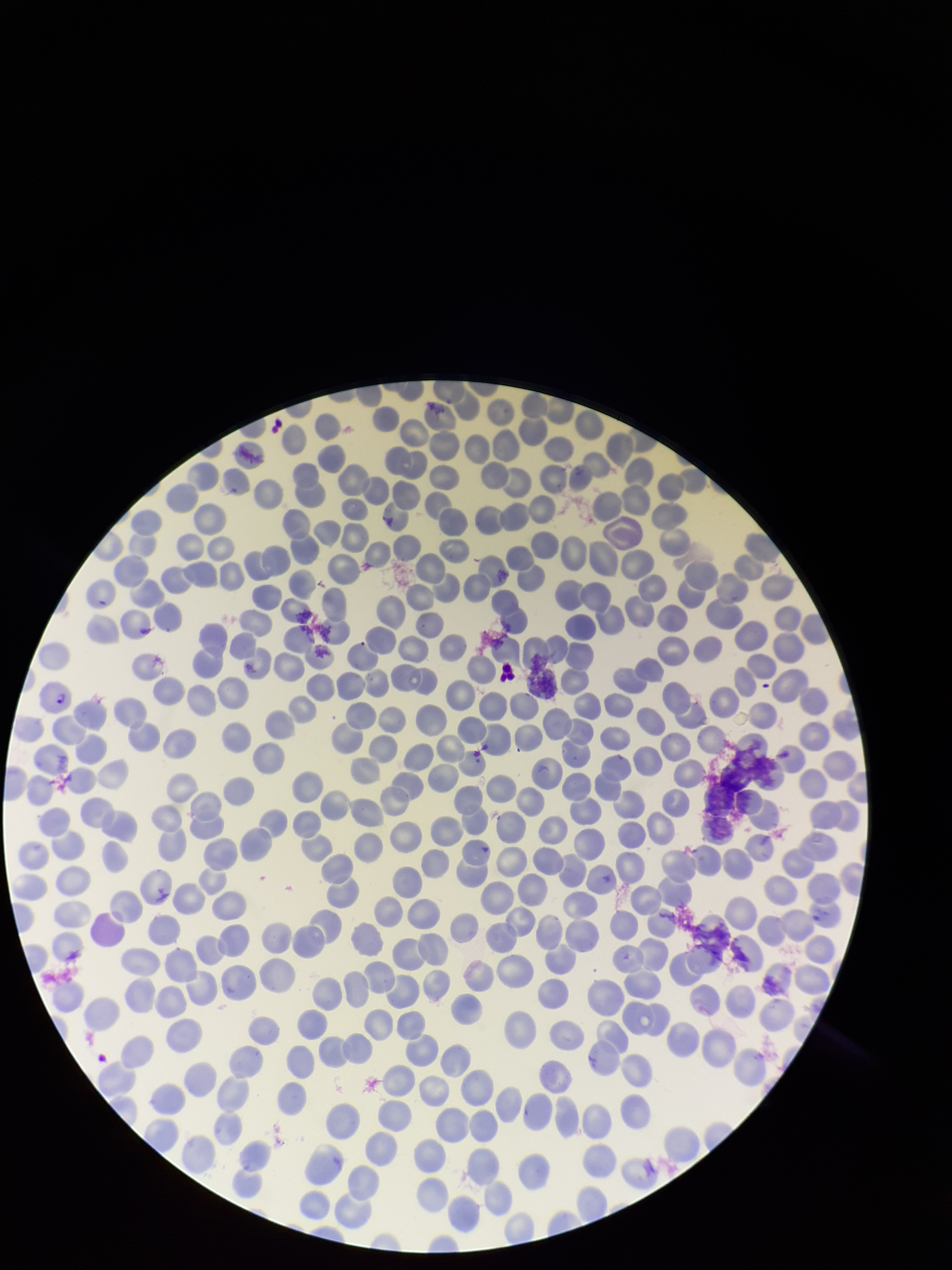
parasitized red blood cell count = 1
patient malaria status = infected
stain = Giemsa
capture = smartphone photograph through the microscope eyepiece
preparation = thin
species reported for this patient = Plasmodium falciparum
parasitized red blood cells = identified
red blood cell count = 363
field of view = one from this slide
image size = 952×1270 pixels